Describe the morphology of the red blood cells.
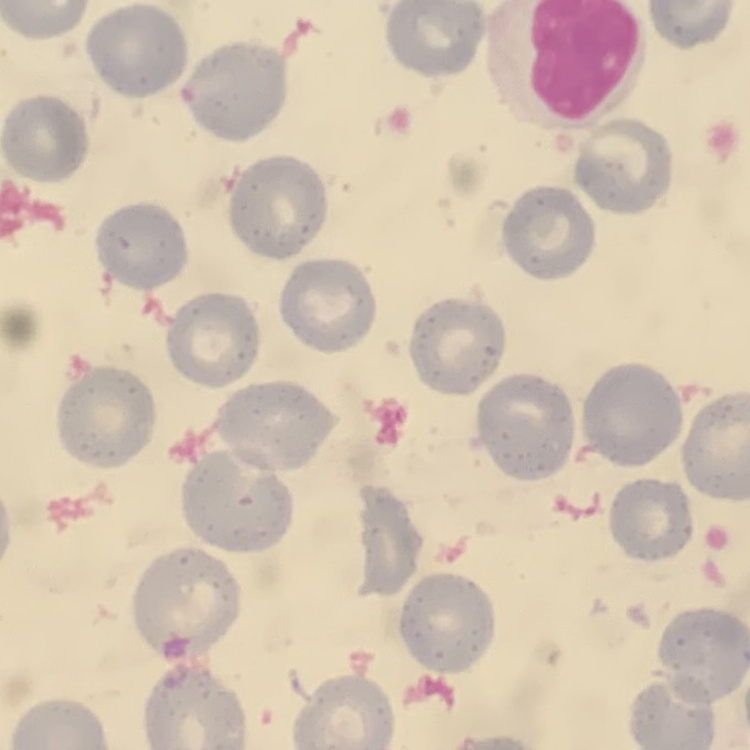

They show no rouleaux formation.

Summary:
  - Image type: square crop of a larger photomicrograph
  - Stain: Field's or Giemsa
  - Preparation: thin blood film